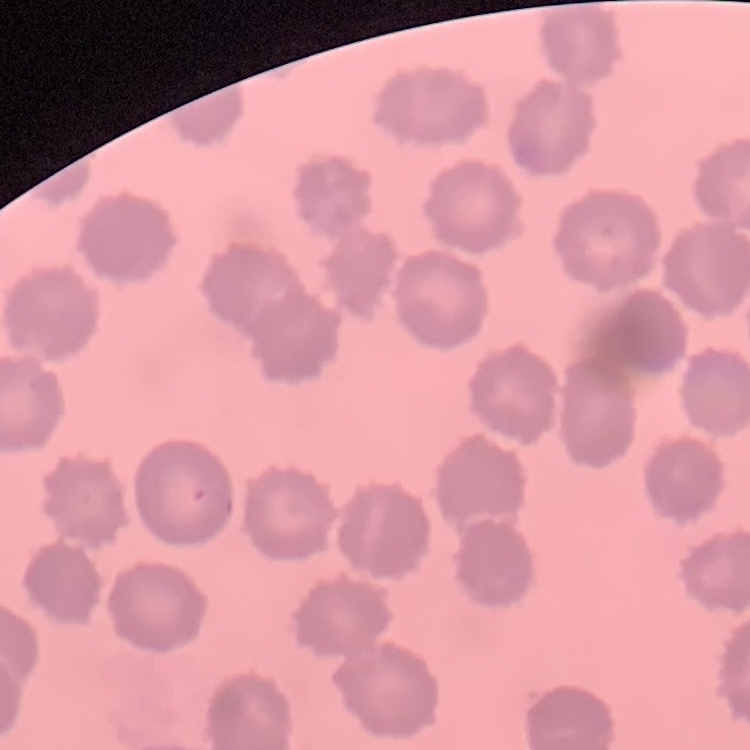
The red blood cells show no rouleaux formation. One tile cut from a larger photomicrograph. Thin blood smear. Stained with either Field's or Giemsa.